Report the malaria status of this cell.
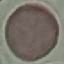

It is uninfected.

{
  "preparation": "thin blood film",
  "image_type": "cell patch, automatically extracted from a larger field of view and resized to 64 × 64 pixels",
  "stain": "Giemsa",
  "capture": "smartphone camera at the microscope eyepiece"
}